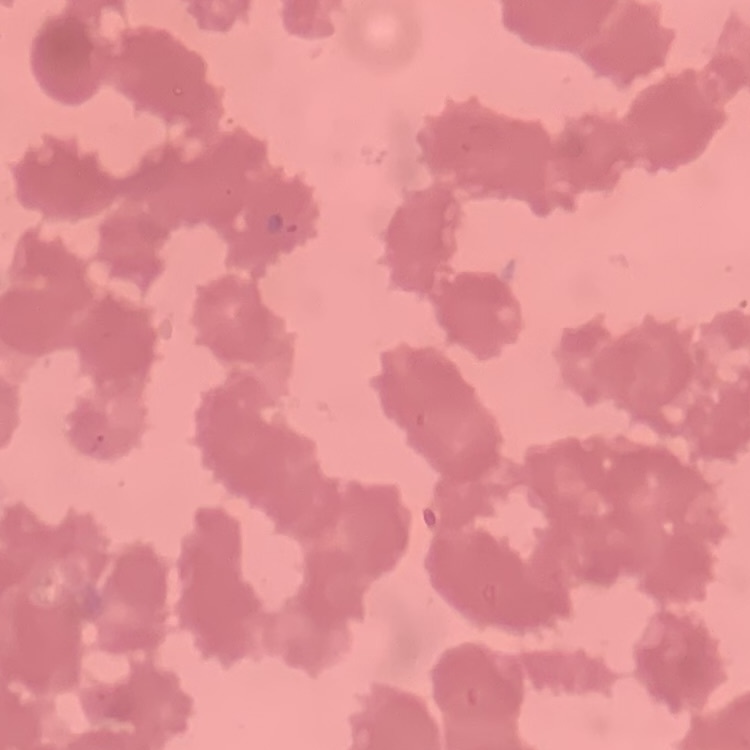

red_blood_cell_morphology: rouleaux formation
stain: Field's or Giemsa
preparation: thin blood smear
image_type: one tile cut from a larger photomicrograph